Locate and identify every blood parasite.
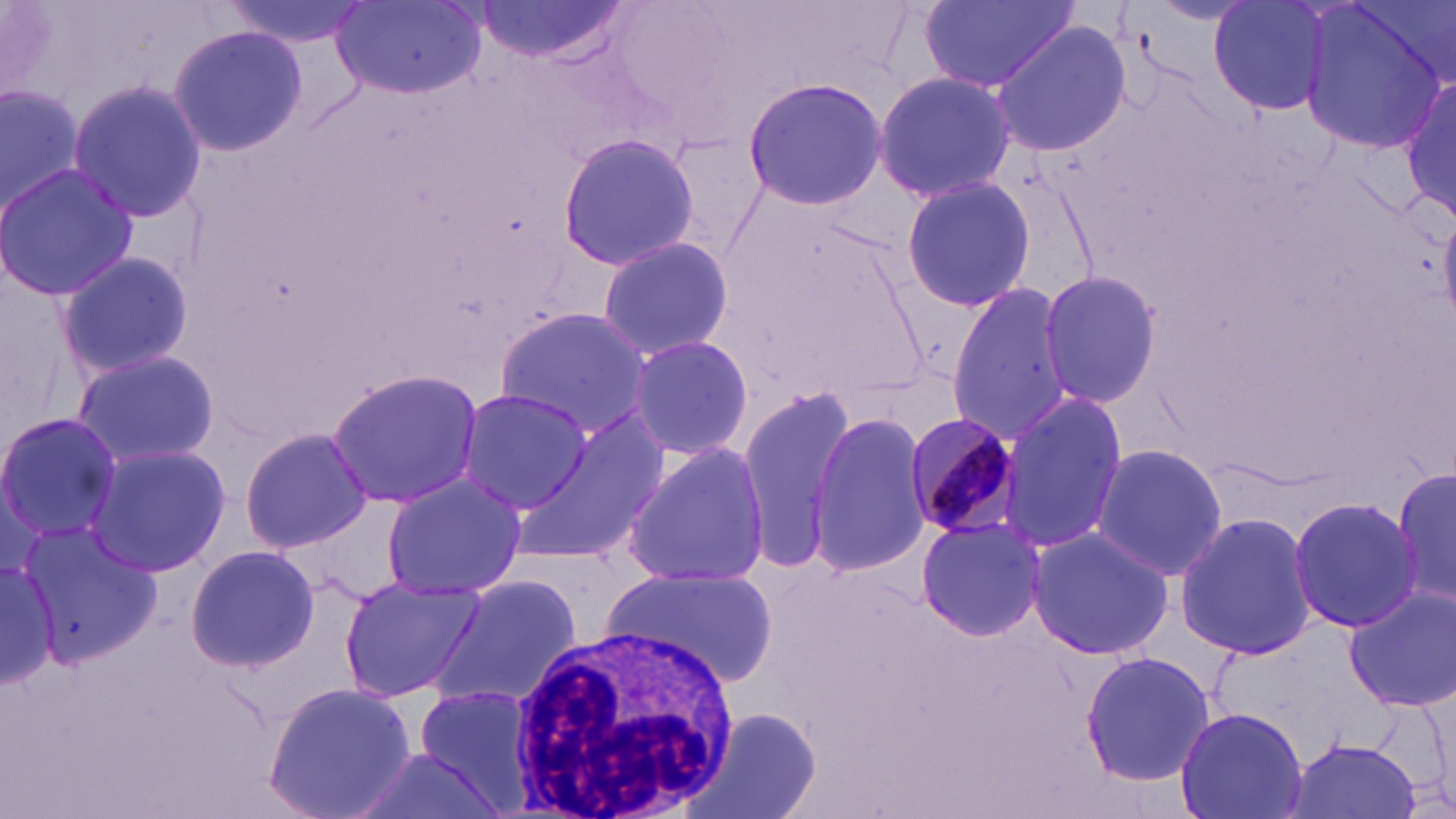

Approximate bounding boxes as [x1, y1, x2, y2] in pixels.
Plasmodium malariae-infected red blood cells: [902, 408, 1026, 545].
No Plasmodium falciparum, Plasmodium ovale, Plasmodium vivax, Babesia divergens, or Trypanosoma brucei observed.

Uninfected red blood cell locations: [3, 0, 54, 101], [221, 0, 373, 47], [479, 0, 626, 63], [915, 0, 1079, 96], [1209, 0, 1335, 118], [1299, 1, 1451, 149], [331, 3, 483, 98], [991, 21, 1133, 156], [169, 25, 307, 155], [874, 70, 1019, 204], [1402, 76, 1456, 221], [739, 78, 888, 210], [0, 80, 85, 214], [69, 80, 205, 224], [661, 131, 771, 260], [555, 132, 699, 271], [0, 161, 138, 304], [900, 175, 1035, 313], [594, 236, 734, 360], [55, 248, 193, 380], [1038, 270, 1163, 407], [946, 281, 1074, 441], [495, 308, 652, 438], [623, 334, 753, 462], [73, 348, 220, 467], [326, 369, 485, 508], [734, 385, 857, 566], [455, 386, 594, 515], [996, 387, 1126, 557], [517, 409, 670, 571], [0, 411, 122, 545], [808, 411, 932, 575], [241, 426, 373, 555], [84, 442, 230, 577], [622, 442, 774, 588], [1090, 443, 1228, 579], [1390, 458, 1454, 614], [380, 473, 526, 601], [1285, 493, 1426, 633], [1174, 512, 1321, 660], [916, 514, 1045, 642], [18, 518, 159, 667], [1027, 526, 1173, 661], [185, 545, 319, 673], [0, 560, 59, 688], [597, 565, 777, 693], [337, 574, 483, 703], [431, 576, 581, 708], [1343, 583, 1456, 712], [1079, 649, 1214, 787], [263, 681, 414, 819], [405, 685, 542, 808], [1174, 706, 1307, 819], [691, 708, 822, 819], [1285, 736, 1425, 819], [347, 745, 504, 819]. White blood cell locations: [508, 619, 745, 819]. Slide-level diagnosis: Plasmodium malariae. May-Grünwald-Giemsa stain. Optical microscopy. 1000x magnification. Image is 1456×819 pixels. One field of a larger specimen. Thin blood film.